Describe the morphology of the erythrocytes.
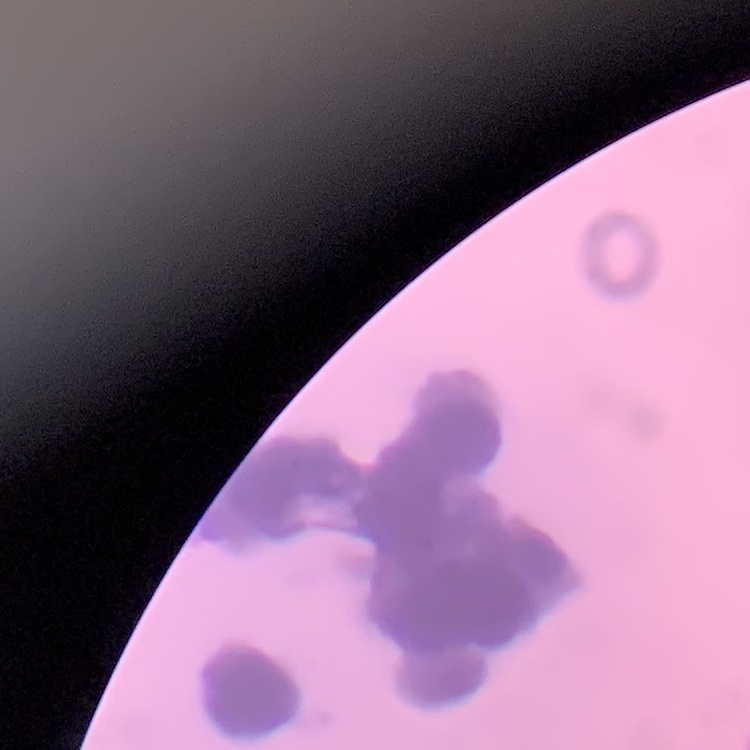
They show rouleaux formation.

{
  "image_type": "one tile cut from a larger photomicrograph",
  "preparation": "thin peripheral smear",
  "stain": "Field's or Giemsa"
}